Identify the parasite.
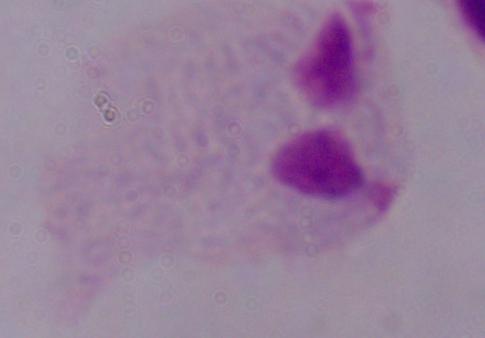
This is a trichomonad.

1000x magnification. Micrograph.